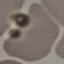
Summary:
  - Malaria status: uninfected
  - Stain: Giemsa
  - Image type: automatically extracted cell patch, resized to 64 × 64 pixels
  - Capture: smartphone through the microscope eyepiece
  - Preparation: thin blood film